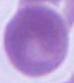 Micrograph. An erythrocyte is seen. Captured at 1000x magnification.